Outline each blood parasite and name the species.
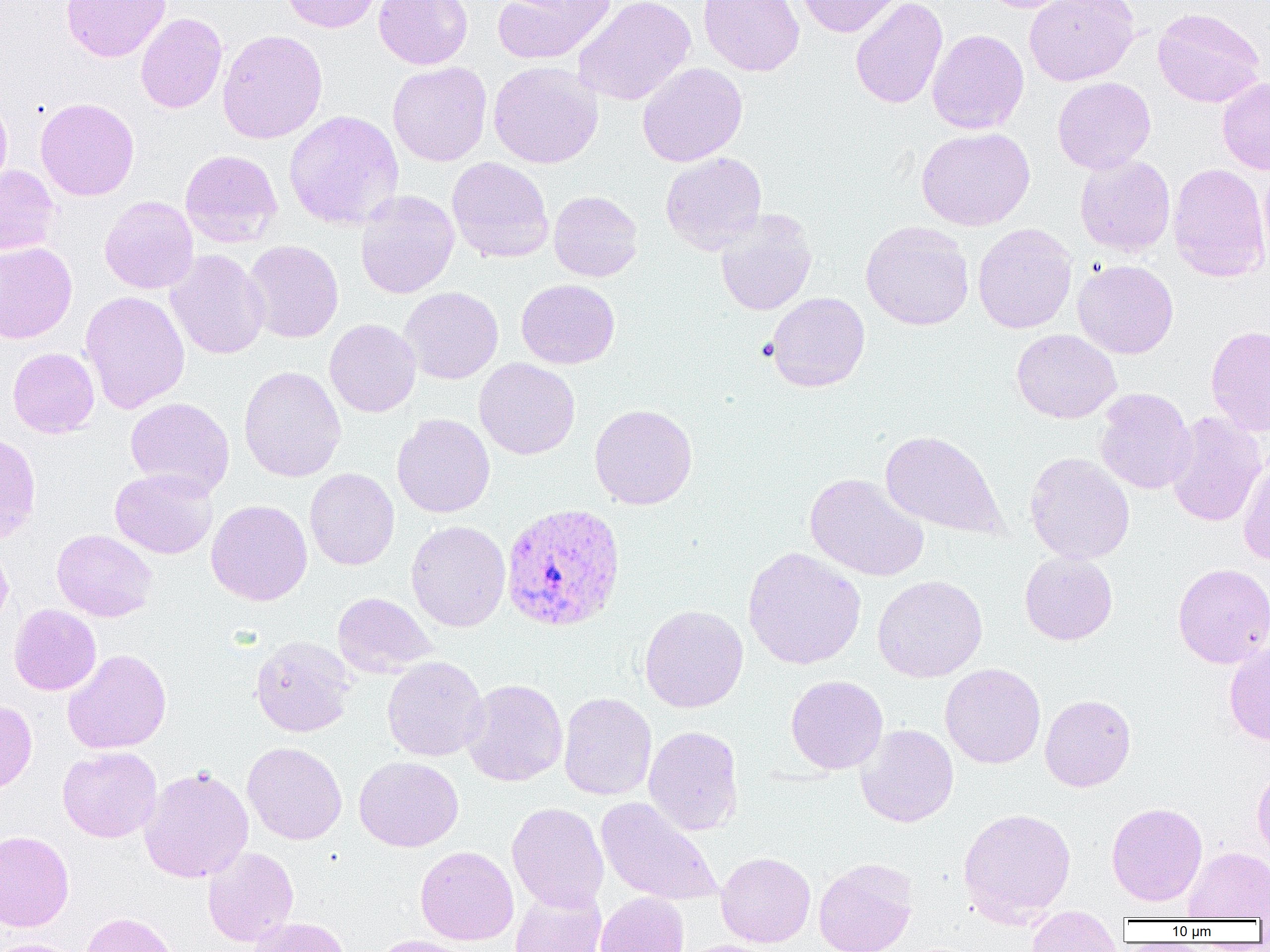

Approximate bounding boxes as named x1/y1/x2/y2 corners in pixels.
Plasmodium vivax-infected red blood cells: (x1=500, y1=502, x2=626, y2=632).
No Plasmodium falciparum, Plasmodium ovale, Plasmodium malariae, Babesia divergens, or Trypanosoma brucei observed.

{
  "slide_level_diagnosis": "Plasmodium vivax",
  "platelet_locations": "approximate bounding boxes as named x1/y1/x2/y2 corners in pixels: (x1=756, y1=337, x2=778, y2=362)",
  "preparation": "thin blood film",
  "image_size": "1270×952 pixels",
  "modality": "optical microscopy",
  "field_of_view": "one of a larger specimen",
  "uninfected_red_blood_cell_locations": "approximate bounding boxes as named x1/y1/x2/y2 corners in pixels: (x1=61, y1=0, x2=170, y2=62), (x1=281, y1=0, x2=382, y2=33), (x1=374, y1=0, x2=473, y2=69), (x1=492, y1=0, x2=616, y2=64), (x1=573, y1=0, x2=695, y2=106), (x1=697, y1=0, x2=804, y2=76), (x1=794, y1=0, x2=905, y2=38), (x1=850, y1=0, x2=947, y2=109), (x1=979, y1=0, x2=1075, y2=13), (x1=1024, y1=0, x2=1139, y2=86), (x1=1153, y1=8, x2=1265, y2=108), (x1=135, y1=13, x2=227, y2=114), (x1=217, y1=29, x2=328, y2=145), (x1=927, y1=29, x2=1029, y2=134), (x1=488, y1=61, x2=603, y2=168), (x1=387, y1=62, x2=491, y2=166), (x1=637, y1=63, x2=748, y2=167), (x1=1052, y1=76, x2=1156, y2=174), (x1=1217, y1=77, x2=1270, y2=176), (x1=0, y1=94, x2=12, y2=197), (x1=35, y1=98, x2=139, y2=201), (x1=284, y1=109, x2=404, y2=231), (x1=916, y1=127, x2=1035, y2=231), (x1=180, y1=150, x2=282, y2=247), (x1=660, y1=152, x2=767, y2=254), (x1=1074, y1=154, x2=1175, y2=256), (x1=447, y1=157, x2=554, y2=264), (x1=1259, y1=162, x2=1270, y2=274), (x1=1168, y1=163, x2=1269, y2=283), (x1=0, y1=165, x2=60, y2=256), (x1=355, y1=190, x2=458, y2=299), (x1=548, y1=190, x2=643, y2=282), (x1=99, y1=196, x2=199, y2=294), (x1=715, y1=210, x2=817, y2=316), (x1=861, y1=221, x2=974, y2=330), (x1=973, y1=223, x2=1077, y2=334), (x1=243, y1=240, x2=344, y2=343), (x1=0, y1=241, x2=77, y2=344), (x1=165, y1=249, x2=270, y2=360), (x1=1072, y1=259, x2=1179, y2=359), (x1=516, y1=279, x2=619, y2=369), (x1=399, y1=287, x2=503, y2=384), (x1=80, y1=290, x2=190, y2=413), (x1=767, y1=292, x2=870, y2=392), (x1=324, y1=319, x2=421, y2=417), (x1=1205, y1=325, x2=1270, y2=436), (x1=1012, y1=329, x2=1122, y2=424), (x1=8, y1=347, x2=99, y2=438), (x1=474, y1=357, x2=580, y2=460), (x1=239, y1=365, x2=346, y2=482), (x1=1094, y1=388, x2=1196, y2=494), (x1=125, y1=397, x2=235, y2=497), (x1=589, y1=404, x2=697, y2=510), (x1=1165, y1=411, x2=1267, y2=527), (x1=391, y1=414, x2=495, y2=518), (x1=880, y1=430, x2=1008, y2=540), (x1=0, y1=432, x2=42, y2=544), (x1=1025, y1=452, x2=1135, y2=564), (x1=1237, y1=456, x2=1270, y2=567), (x1=110, y1=468, x2=218, y2=559), (x1=305, y1=468, x2=399, y2=570), (x1=804, y1=472, x2=930, y2=582), (x1=206, y1=500, x2=312, y2=606), (x1=406, y1=520, x2=510, y2=632), (x1=51, y1=529, x2=158, y2=622), (x1=0, y1=539, x2=13, y2=630), (x1=743, y1=547, x2=866, y2=670), (x1=1019, y1=551, x2=1118, y2=645), (x1=1172, y1=563, x2=1270, y2=668), (x1=872, y1=574, x2=988, y2=682), (x1=332, y1=592, x2=436, y2=677), (x1=9, y1=604, x2=101, y2=696), (x1=639, y1=604, x2=748, y2=713), (x1=250, y1=635, x2=356, y2=737), (x1=1224, y1=642, x2=1270, y2=746), (x1=62, y1=648, x2=172, y2=754), (x1=382, y1=656, x2=489, y2=761), (x1=940, y1=663, x2=1045, y2=768), (x1=786, y1=675, x2=888, y2=774), (x1=461, y1=679, x2=568, y2=787), (x1=558, y1=692, x2=657, y2=800), (x1=1040, y1=694, x2=1136, y2=792), (x1=0, y1=699, x2=37, y2=795), (x1=856, y1=724, x2=959, y2=828), (x1=643, y1=725, x2=744, y2=836), (x1=242, y1=741, x2=346, y2=845), (x1=58, y1=746, x2=161, y2=842), (x1=354, y1=756, x2=464, y2=852), (x1=139, y1=766, x2=253, y2=883), (x1=1252, y1=767, x2=1270, y2=860), (x1=596, y1=797, x2=723, y2=907), (x1=507, y1=802, x2=609, y2=913), (x1=1106, y1=802, x2=1208, y2=906), (x1=957, y1=807, x2=1077, y2=926), (x1=0, y1=830, x2=74, y2=932), (x1=203, y1=846, x2=299, y2=947), (x1=415, y1=846, x2=519, y2=945), (x1=1183, y1=846, x2=1270, y2=920), (x1=716, y1=852, x2=816, y2=947), (x1=814, y1=857, x2=918, y2=952), (x1=510, y1=887, x2=606, y2=952), (x1=595, y1=892, x2=690, y2=952), (x1=1025, y1=910, x2=1123, y2=952), (x1=80, y1=912, x2=182, y2=952), (x1=248, y1=917, x2=351, y2=952), (x1=369, y1=935, x2=476, y2=952), (x1=0, y1=938, x2=84, y2=952), (x1=676, y1=939, x2=784, y2=952)",
  "magnification": "1000x"
}